Locate every leukocyte (white blood cell).
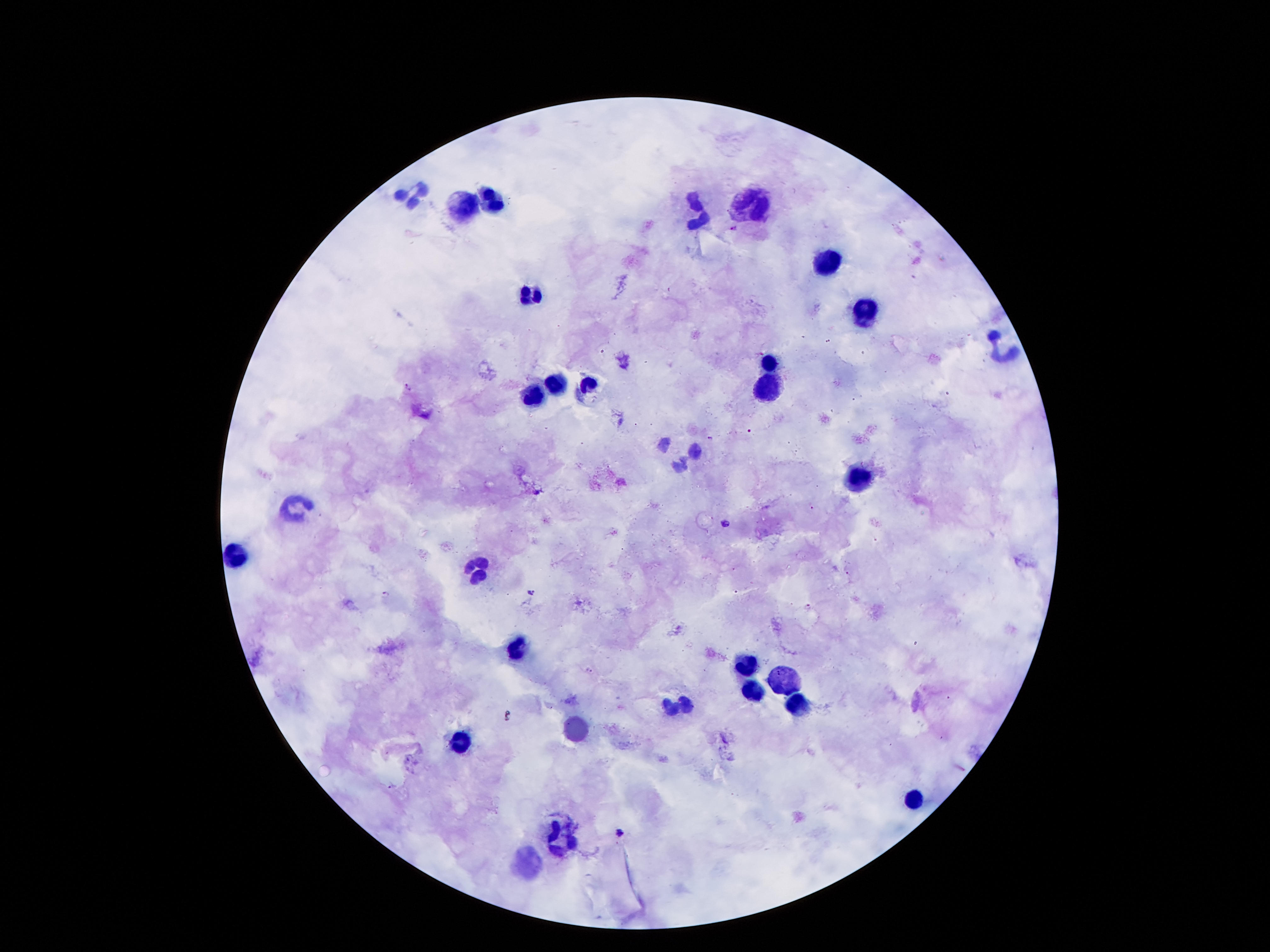

Approximate centers as {x, y} in pixels.
Leukocytes: {415, 196}, {490, 196}, {749, 203}, {461, 205}, {699, 212}, {826, 262}, {527, 292}, {863, 310}, {1001, 345}, {768, 362}, {558, 382}, {590, 385}, {768, 391}, {533, 398}, {860, 474}, {297, 505}, {238, 551}, {475, 562}, {515, 650}, {747, 663}, {785, 675}, {752, 693}, {681, 704}, {795, 706}, {459, 745}, {911, 800}, {559, 837}, {531, 866}.

Summary:
  - Plasmodium parasite locations: {733, 228}, {408, 386}, {710, 437}, {813, 508}, {726, 524}, {847, 573}, {531, 593}, {386, 595}, {808, 607}, {589, 671}, {392, 786}, {621, 832}
  - Patient malaria status: infected with Plasmodium falciparum
  - Field of view: single
  - Magnification: 100x
  - Capture: smartphone through the microscope eyepiece
  - Preparation: thick blood film
  - Stain: Giemsa
  - Image size: 1270×952 pixels